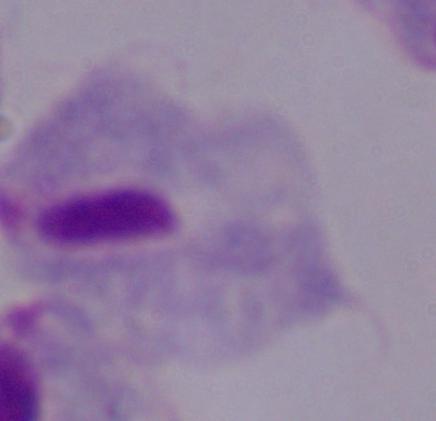

Summary:
  - Modality: photomicrograph
  - Magnification: 1000x
  - Identification: trichomonad